Classify this cell by malaria status.
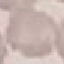

It is uninfected.

Automatically extracted cell patch, resized to 64 × 64 pixels. Giemsa stain. Thin blood smear. Acquired by smartphone through the microscope eyepiece.